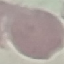

{
  "malaria_status": "uninfected",
  "preparation": "thin blood smear",
  "image_type": "automatically extracted cell patch, resized to 64 × 64 pixels",
  "capture": "smartphone through the microscope eyepiece",
  "stain": "Giemsa"
}